Classify this cell by malaria status.
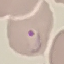
Parasitized.

Thin blood smear. Giemsa stain. Acquired by smartphone through the microscope eyepiece. Cell patch, automatically extracted from a larger field of view and resized to 64 × 64 pixels.